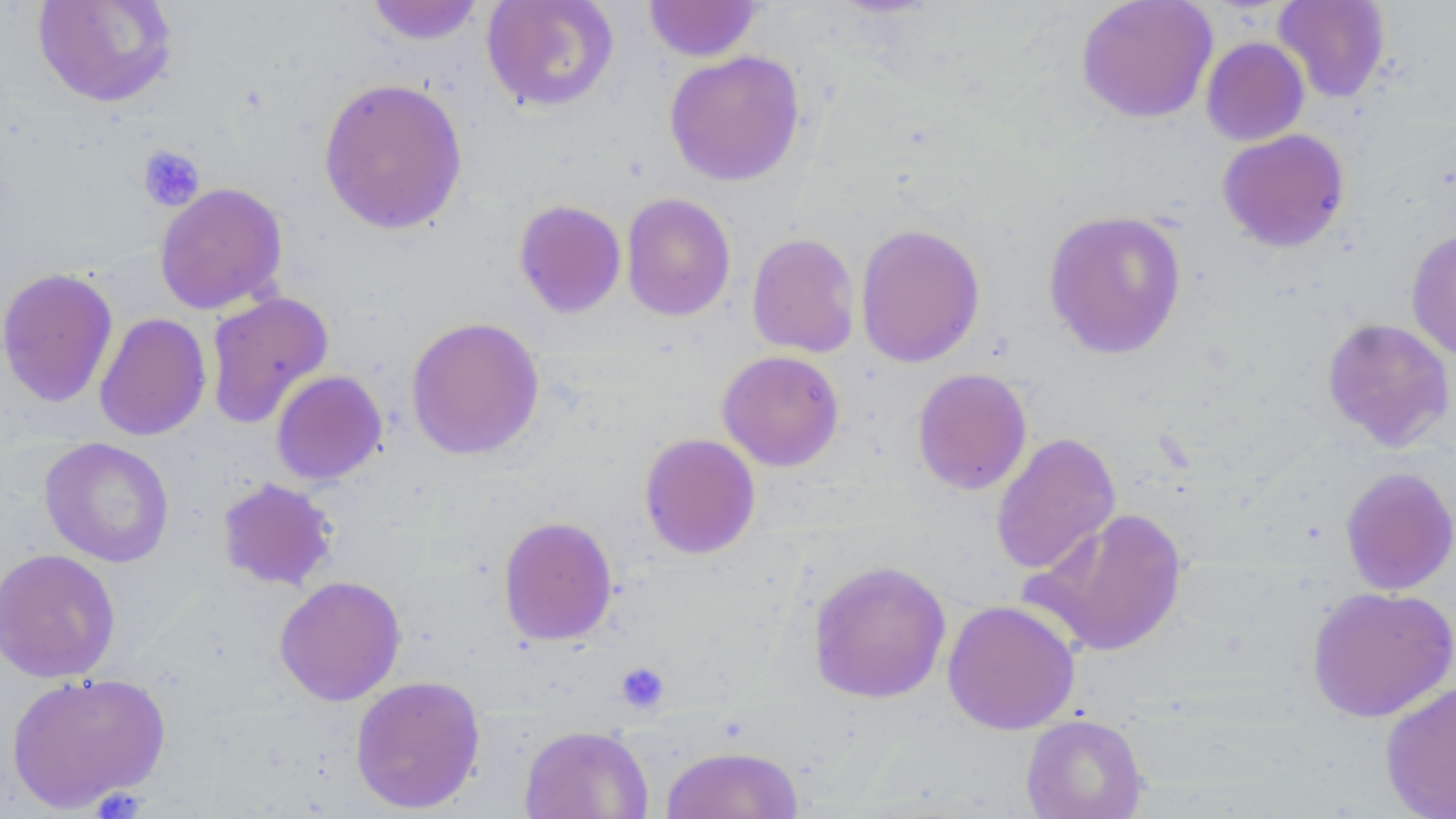
Approximate bounding boxes as [x1, y1, x2, y2] in pixels. Uninfected red blood cell locations: [32, 0, 179, 109], [481, 0, 620, 114], [1075, 0, 1217, 124], [1273, 0, 1392, 103], [363, 1, 488, 46], [643, 1, 764, 62], [1200, 37, 1309, 146], [663, 50, 806, 187], [317, 76, 468, 236], [1217, 129, 1350, 253], [154, 182, 288, 315], [621, 193, 736, 321], [513, 199, 627, 319], [1042, 209, 1188, 360], [855, 223, 986, 368], [1406, 229, 1456, 362], [746, 232, 861, 358], [0, 267, 119, 408], [205, 290, 334, 429], [94, 312, 212, 442], [405, 315, 545, 461], [1322, 317, 1455, 451], [717, 350, 844, 471], [912, 367, 1033, 495], [270, 370, 388, 486], [639, 432, 761, 560], [990, 432, 1121, 576], [39, 437, 175, 568], [1339, 466, 1456, 596], [215, 477, 340, 592], [1029, 506, 1188, 658], [497, 515, 618, 646], [0, 548, 121, 683], [807, 559, 951, 704], [274, 575, 407, 706], [1306, 585, 1456, 723], [942, 599, 1081, 736], [5, 670, 171, 812], [349, 674, 486, 814], [1380, 680, 1456, 819], [1020, 713, 1148, 819], [518, 723, 653, 819], [660, 744, 804, 818]. Platelet locations: [137, 145, 205, 211], [615, 662, 670, 713]. Slide-level diagnosis: no evidence of blood parasites. Thin blood film. Image is 1456×819 pixels. May-Grünwald-Giemsa-stained preparation. Single field of view. Captured at 1000x magnification. Light microscopy.